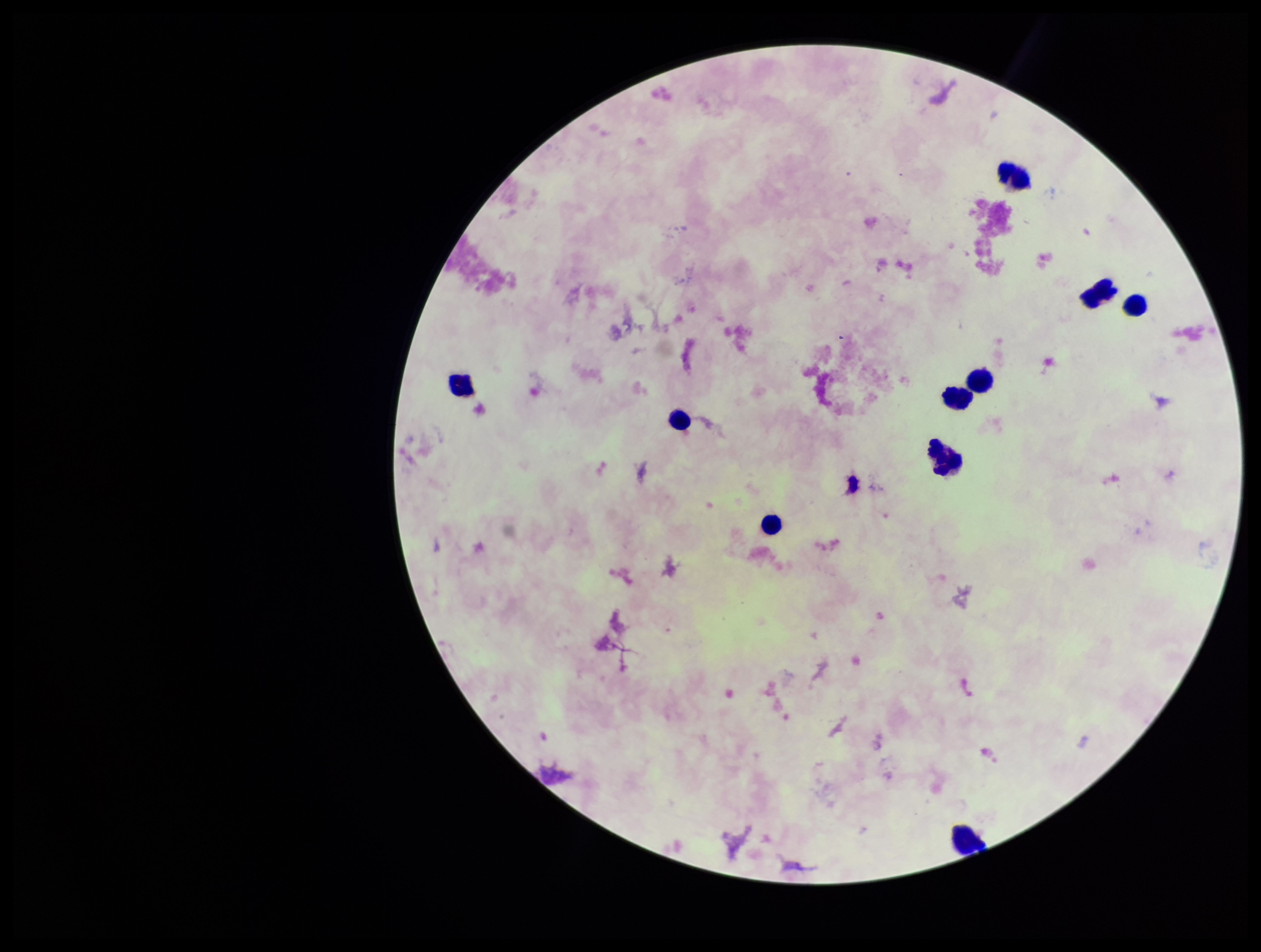

Plasmodium parasites = none detected
preparation = thick smear
image size = 1261×952 pixels
field of view = one from this slide
patient malaria status = negative
leukocyte count = 10
capture = smartphone photograph through the microscope eyepiece
parasite count = 0
stain = Giemsa